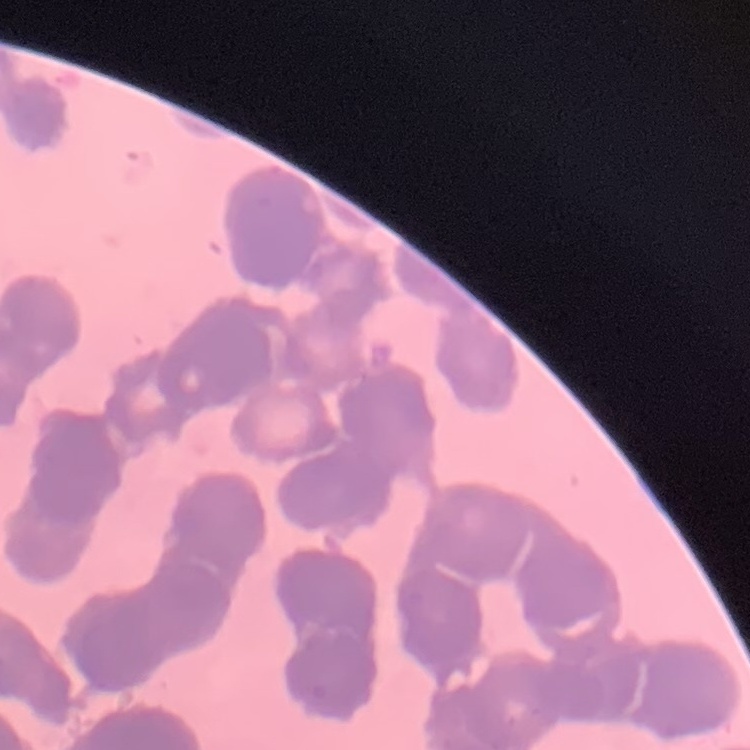

red blood cell morphology = rouleaux formation
image type = one tile cut from a larger photomicrograph
stain = Field's or Giemsa
preparation = thin blood film